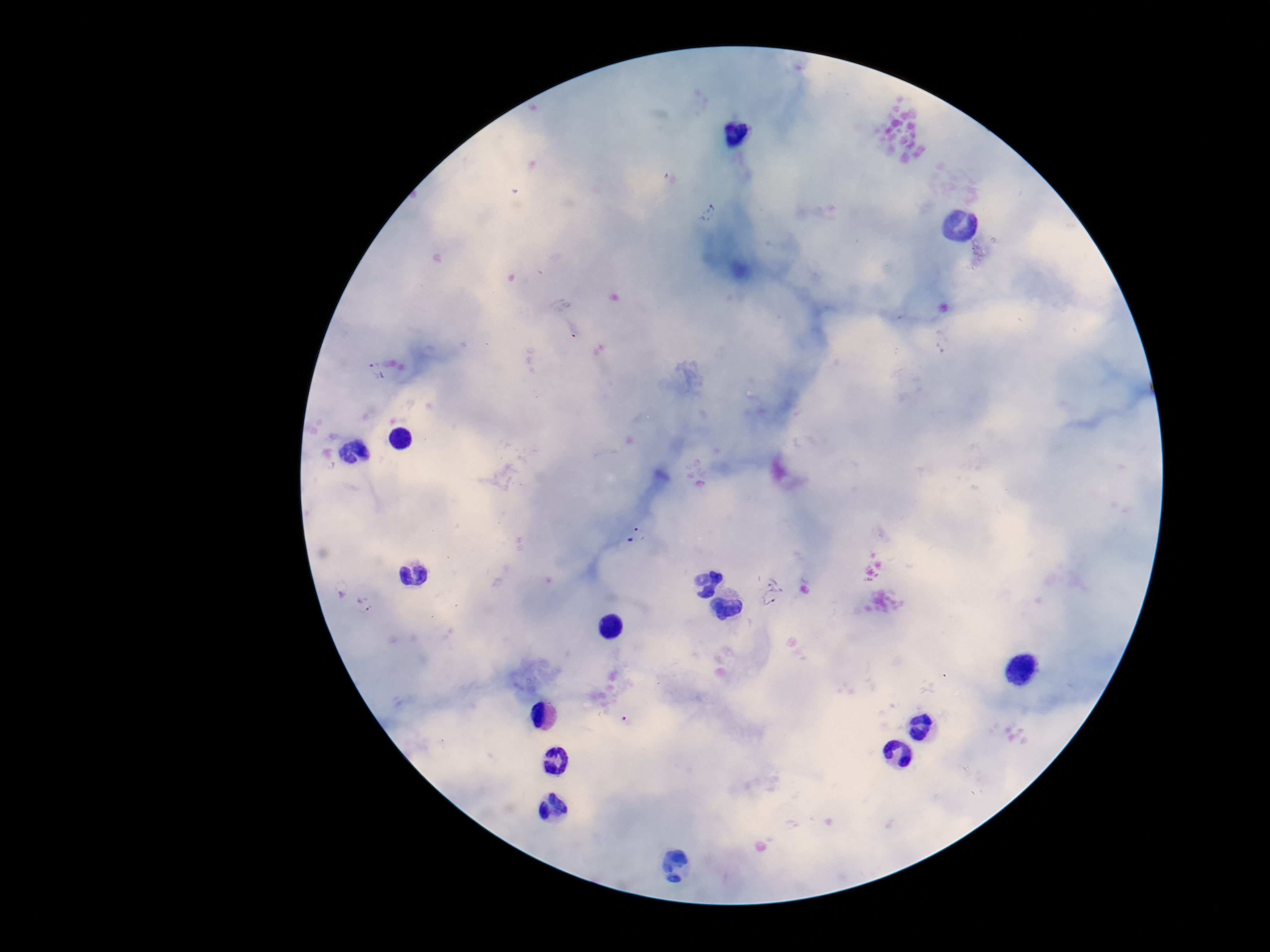

Approximate object centers, in pixels from the top-left corner. Plasmodium parasite locations: (x=709, y=214), (x=375, y=371), (x=635, y=535), (x=772, y=592), (x=364, y=605). Thick blood film. Patient malaria status: positive. Giemsa-stained preparation. 100x magnification. Image is 1270×952 pixels. Single field of view. Smartphone photograph taken through the microscope eyepiece.